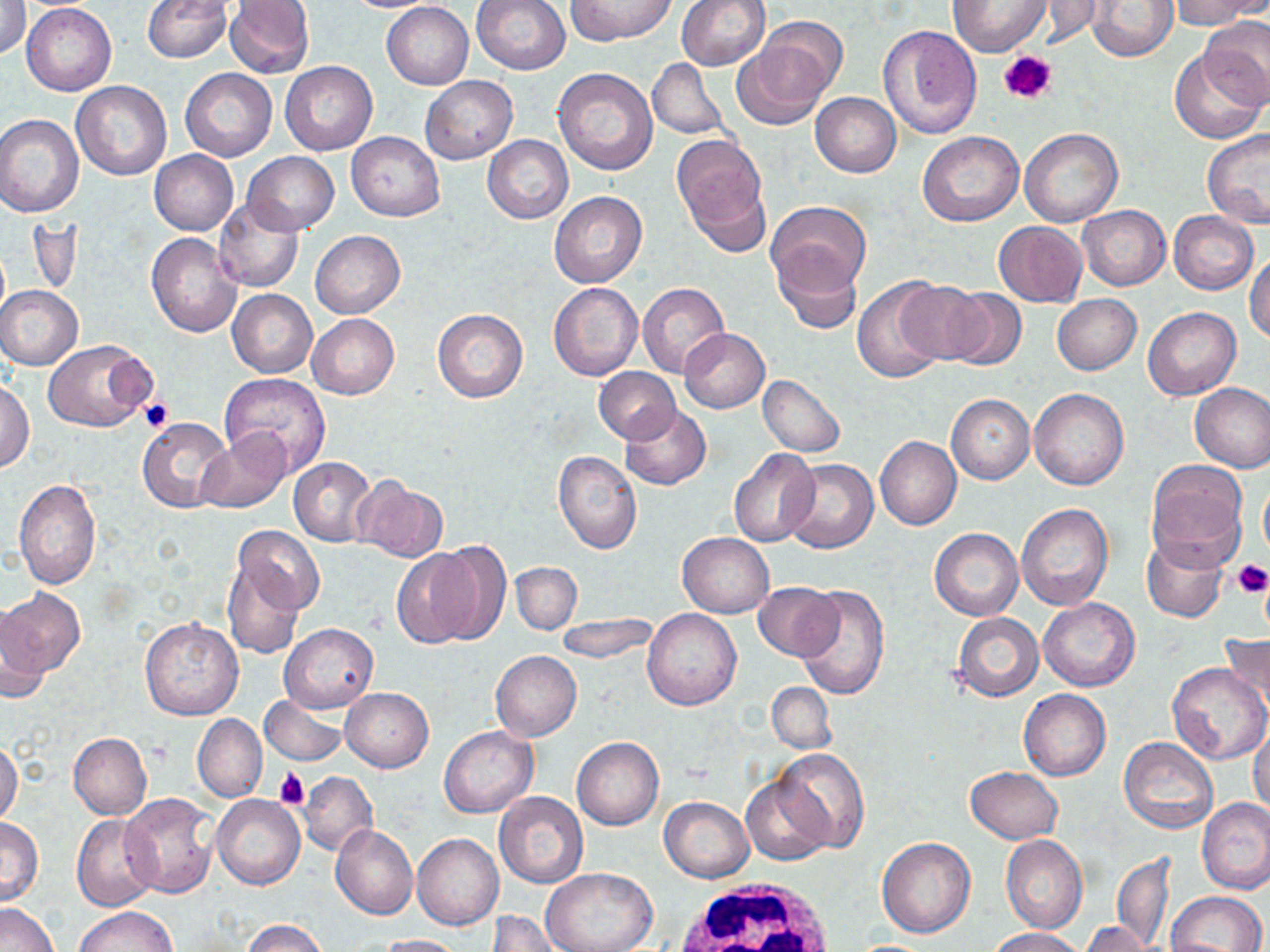

Summary:
  - Coordinate format: approximate bounding boxes as (x1, y1, x2, y2) in pixels
  - Uninfected red blood cell locations: (142, 0, 232, 62), (223, 0, 315, 79), (339, 0, 446, 12), (566, 0, 676, 45), (675, 0, 770, 70), (1170, 0, 1264, 30), (470, 1, 571, 75), (947, 1, 1051, 56), (1023, 1, 1105, 48), (1086, 1, 1178, 62), (1, 2, 31, 60), (381, 2, 473, 89), (22, 4, 115, 95), (759, 17, 848, 104), (1201, 19, 1270, 111), (877, 25, 981, 140), (732, 37, 834, 129), (1168, 48, 1267, 144), (647, 58, 729, 141), (279, 61, 376, 155), (553, 67, 658, 175), (181, 70, 276, 161), (419, 75, 517, 165), (71, 81, 172, 182), (810, 92, 901, 177), (0, 115, 83, 217), (1020, 128, 1123, 227), (1201, 129, 1270, 228), (347, 131, 444, 221), (917, 132, 1025, 227), (670, 134, 769, 241), (483, 135, 572, 223), (149, 150, 237, 236), (243, 152, 338, 235), (549, 192, 647, 288), (214, 196, 304, 293), (766, 200, 872, 299), (1077, 205, 1170, 290), (1169, 211, 1258, 294), (993, 221, 1087, 307), (310, 231, 404, 318), (146, 233, 243, 337), (773, 249, 864, 334), (1247, 251, 1270, 343), (853, 278, 949, 382), (549, 281, 643, 380), (893, 281, 990, 365), (637, 282, 729, 377), (0, 286, 83, 370), (940, 288, 1027, 372), (228, 289, 316, 377), (1051, 294, 1141, 374), (432, 307, 528, 403), (1143, 307, 1242, 400), (307, 313, 399, 400), (679, 328, 770, 412), (43, 338, 154, 432), (594, 367, 682, 444), (219, 372, 331, 476), (757, 375, 846, 458), (0, 380, 33, 472), (1189, 382, 1270, 473), (1028, 390, 1128, 491), (946, 394, 1034, 484), (620, 406, 711, 490), (137, 418, 234, 513), (196, 431, 294, 514), (875, 436, 961, 529), (729, 448, 820, 547), (553, 451, 642, 554), (288, 457, 376, 545), (782, 459, 878, 553), (1146, 459, 1248, 566), (1259, 476, 1270, 565), (354, 477, 447, 562), (13, 478, 102, 589), (1015, 503, 1113, 611), (232, 525, 326, 617), (929, 528, 1023, 621), (678, 533, 773, 617), (1142, 537, 1228, 623), (427, 541, 512, 643), (389, 546, 485, 648), (221, 555, 305, 658), (511, 563, 580, 634), (753, 583, 842, 662), (795, 583, 889, 699), (2, 589, 84, 680), (1038, 597, 1139, 691), (0, 605, 50, 704), (642, 609, 742, 711), (556, 613, 657, 664), (951, 613, 1043, 701), (140, 617, 243, 720), (280, 623, 378, 714), (1219, 634, 1269, 711), (490, 651, 581, 742), (1166, 662, 1268, 765), (767, 682, 835, 755), (340, 687, 433, 772), (1019, 689, 1110, 780), (259, 695, 347, 765), (193, 714, 266, 802), (439, 725, 537, 817), (1249, 725, 1270, 815), (67, 732, 152, 819), (572, 737, 663, 830), (1120, 737, 1217, 833), (0, 738, 22, 827), (770, 749, 869, 852), (964, 767, 1061, 843), (298, 770, 378, 855), (741, 777, 833, 865), (494, 791, 588, 887), (119, 794, 219, 898), (212, 795, 304, 890), (659, 796, 753, 881), (1197, 798, 1270, 894), (72, 813, 160, 910), (0, 817, 42, 906), (331, 824, 417, 921), (412, 834, 503, 930), (1001, 834, 1087, 934), (926, 836, 1074, 946), (876, 837, 976, 937), (1113, 854, 1175, 950), (540, 867, 656, 952), (1166, 891, 1266, 952), (0, 903, 60, 952), (74, 907, 176, 952), (484, 911, 560, 952), (241, 919, 329, 952), (1081, 922, 1159, 952), (987, 928, 1084, 951), (376, 934, 467, 952)
  - White blood cell locations: (669, 880, 840, 952)
  - Platelet locations: (1000, 49, 1057, 106), (139, 396, 174, 433), (1231, 561, 1269, 599), (274, 767, 309, 810)
  - Slide-level diagnosis: negative for blood parasites
  - Field of view: one of a larger specimen
  - Stain: May-Grünwald-Giemsa
  - Magnification: 1000x
  - Image size: 1270×952 pixels
  - Preparation: thin blood film
  - Modality: light microscopy